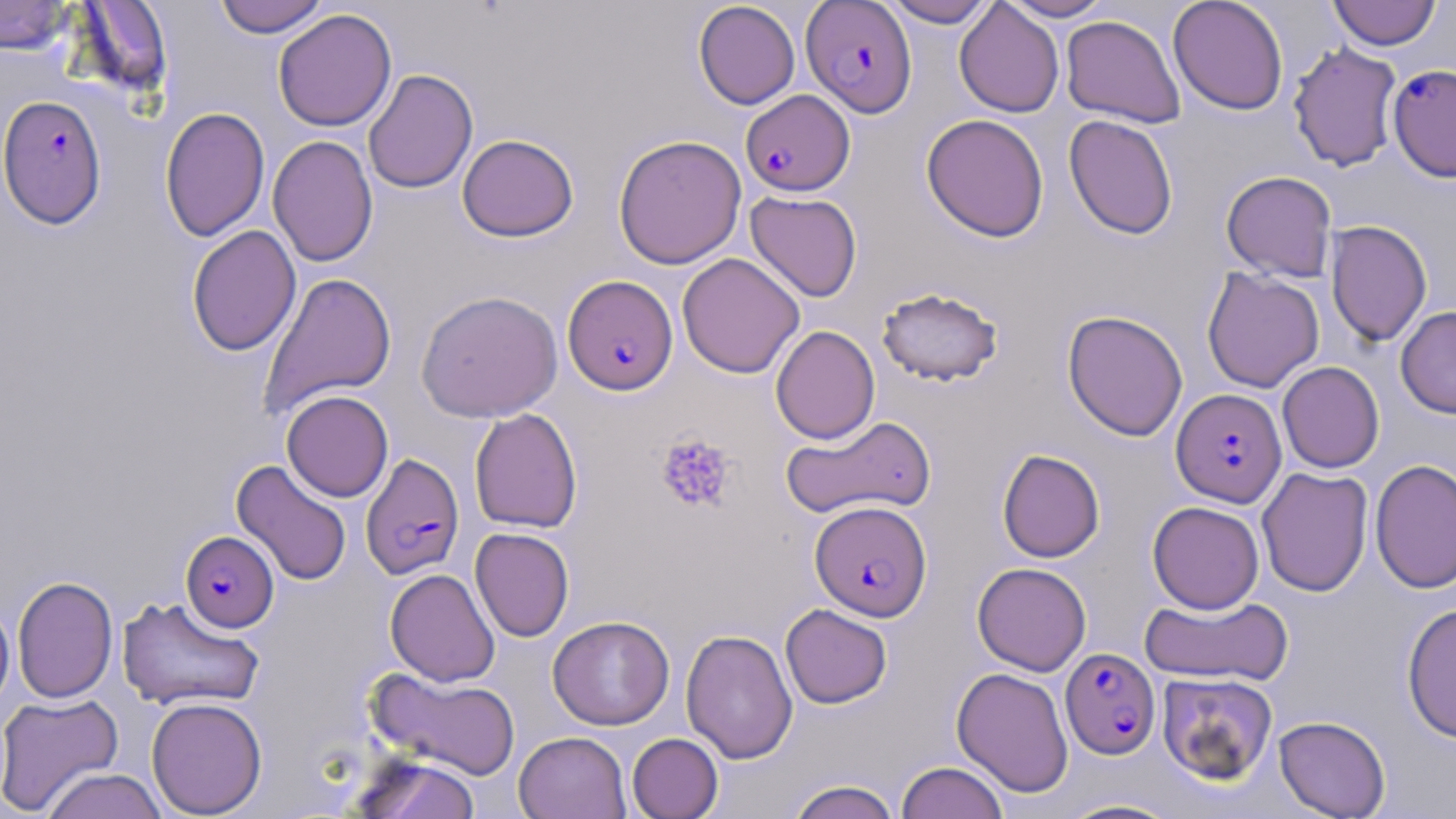
slide_level_diagnosis: Plasmodium falciparum
platelet_locations: 'approximate bounding boxes as (x1, y1, x2, y2) in pixels: (655, 433, 737, 514)'
magnification: 1000x
image_size: 1456×819 pixels
field_of_view: one of a larger specimen
plasmodium_falciparum_infected_red_blood_cell_locations: 'approximate bounding boxes as (x1, y1, x2, y2) in pixels: (801, 0, 917, 117), (1387, 64, 1456, 181), (741, 89, 854, 196), (0, 95, 107, 228), (563, 274, 679, 394), (1171, 388, 1287, 507), (360, 452, 465, 580), (810, 500, 932, 621), (181, 530, 279, 632), (1060, 648, 1160, 759)'
modality: optical microscopy
stain: May-Grünwald-Giemsa
uninfected_red_blood_cell_locations: 'approximate bounding boxes as (x1, y1, x2, y2) in pixels: (213, 0, 330, 38), (880, 0, 999, 27), (1001, 0, 1115, 21), (1168, 0, 1289, 116), (1327, 0, 1441, 50), (0, 1, 75, 55), (69, 1, 174, 99), (693, 2, 800, 109), (954, 2, 1064, 118), (273, 9, 397, 132), (1061, 15, 1185, 128), (1287, 41, 1403, 172), (363, 69, 478, 194), (160, 107, 270, 242), (921, 114, 1049, 242), (1064, 115, 1178, 239), (457, 134, 579, 242), (613, 134, 747, 269), (267, 135, 377, 267), (1221, 170, 1337, 282), (745, 191, 862, 301), (1325, 220, 1432, 347), (187, 225, 302, 357), (677, 253, 805, 378), (1202, 267, 1324, 393), (259, 271, 397, 418), (876, 286, 1004, 387), (416, 290, 563, 422), (1396, 306, 1456, 418), (1062, 310, 1188, 441), (771, 325, 880, 444), (1277, 361, 1384, 473), (281, 390, 394, 502), (469, 407, 583, 533), (781, 415, 936, 520), (997, 449, 1105, 562), (1370, 458, 1456, 593), (231, 459, 352, 587), (1256, 467, 1373, 597), (1147, 501, 1264, 613), (470, 528, 574, 642), (972, 562, 1091, 676), (385, 568, 500, 686), (12, 576, 118, 704), (1139, 593, 1292, 686), (116, 595, 266, 713), (0, 597, 15, 715), (1401, 603, 1456, 743), (780, 604, 892, 708), (547, 615, 674, 730), (681, 628, 798, 764), (364, 666, 521, 782), (952, 667, 1073, 798), (1156, 672, 1278, 785), (0, 692, 122, 815), (146, 697, 268, 817), (1273, 715, 1391, 819), (514, 731, 631, 819), (627, 733, 723, 819), (350, 753, 481, 819), (896, 761, 1009, 819), (41, 767, 168, 819), (785, 779, 902, 819), (1055, 798, 1186, 818)'
preparation: thin blood smear